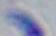
modality: micrograph
identification: Toxoplasma gondii
magnification: 1000x